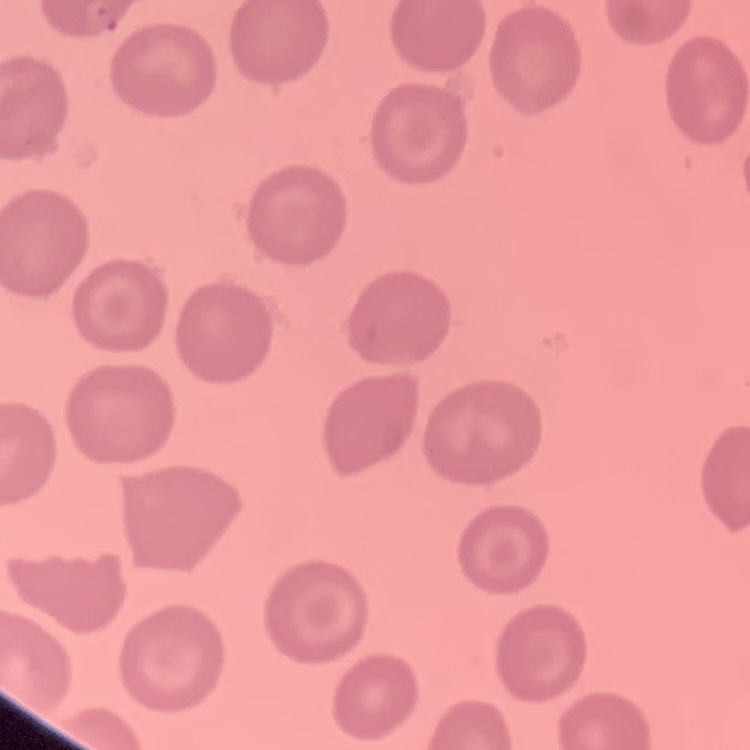
Summary:
  - Red blood cell morphology: no rouleaux formation
  - Preparation: thin blood film
  - Stain: Field's or Giemsa
  - Image type: square crop of a larger photomicrograph